Assess the morphology of the red blood cells.
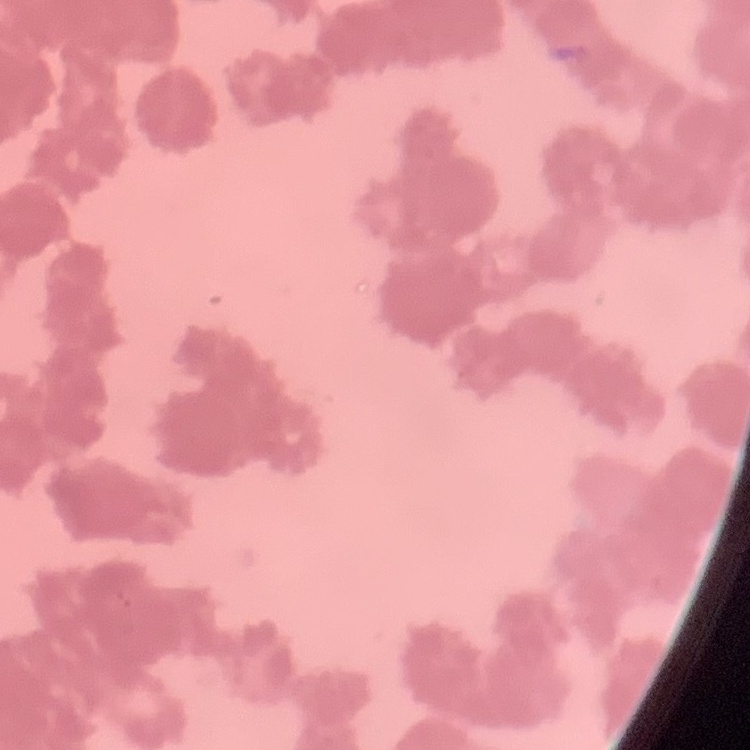
Rouleaux formation.

image_type: square crop of a larger photomicrograph
stain: Field's or Giemsa
preparation: thin blood smear